Classify this cell by malaria status.
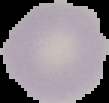
It is uninfected.

image type = segmented cell region with the area outside set to black
image size = 109×103 pixels
preparation = thin blood film